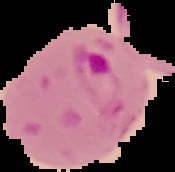
malaria_status: parasitized
image_type: segmented cell region with the area outside set to black
image_size: 175×172 pixels
preparation: thin blood film